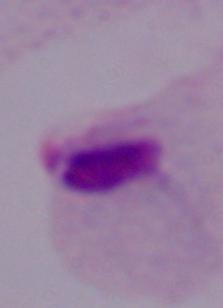

Summary:
  - Magnification: 1000x
  - Modality: micrograph
  - Identification: trichomonad